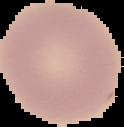

Summary:
  - Preparation: thin blood smear
  - Result: no malaria parasites detected
  - Image type: segmented cell region with the area outside set to black
  - Image size: 124×127 pixels